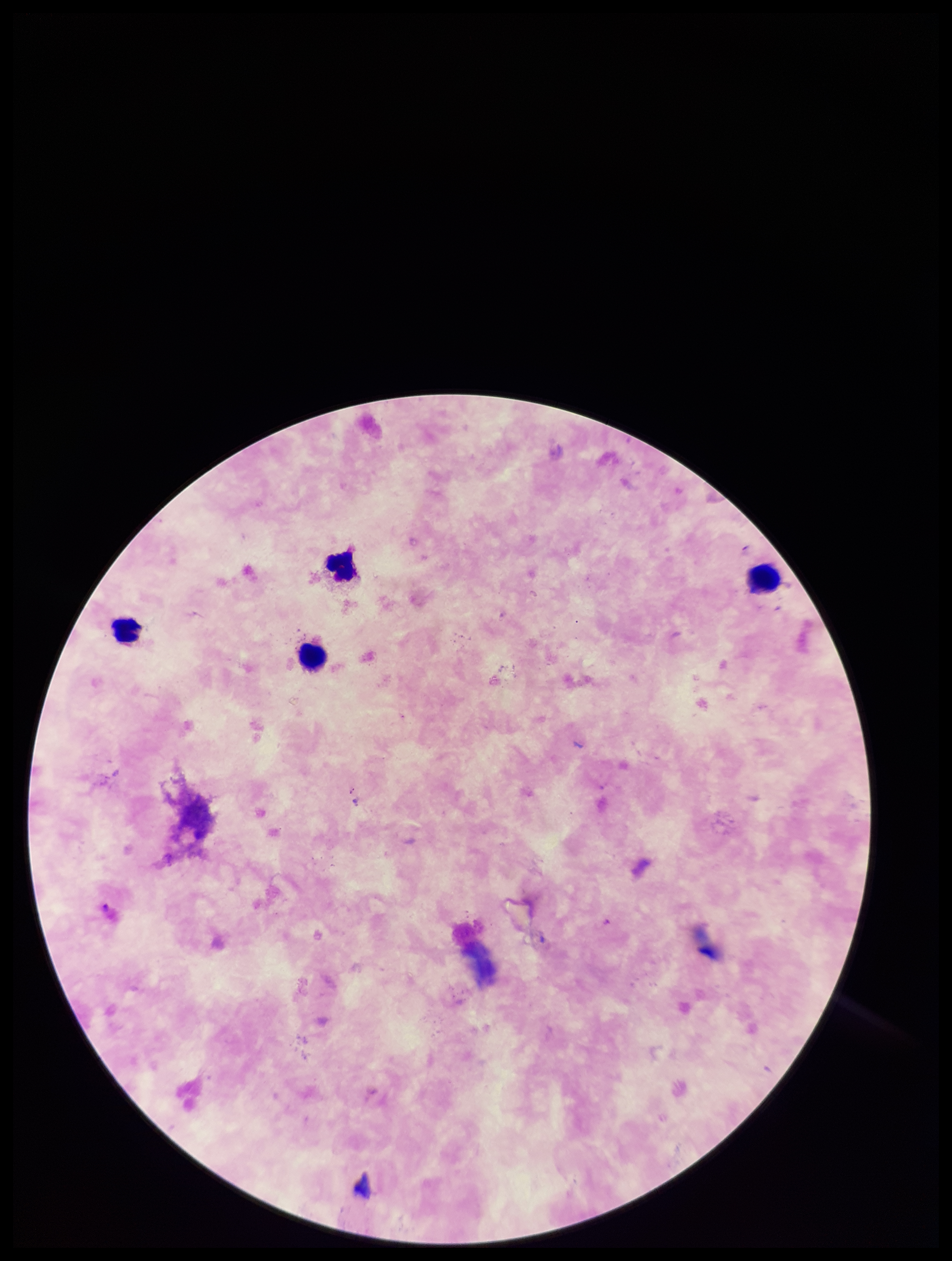
patient malaria status = positive
preparation = thick smear
capture = smartphone photograph through the microscope eyepiece
image size = 952×1261 pixels
leukocyte count = 4
Plasmodium parasites = none identified
parasite count = 0
stain = Giemsa
field of view = one from this slide
species reported for this patient = Plasmodium falciparum